Comment on the morphology of the erythrocytes.
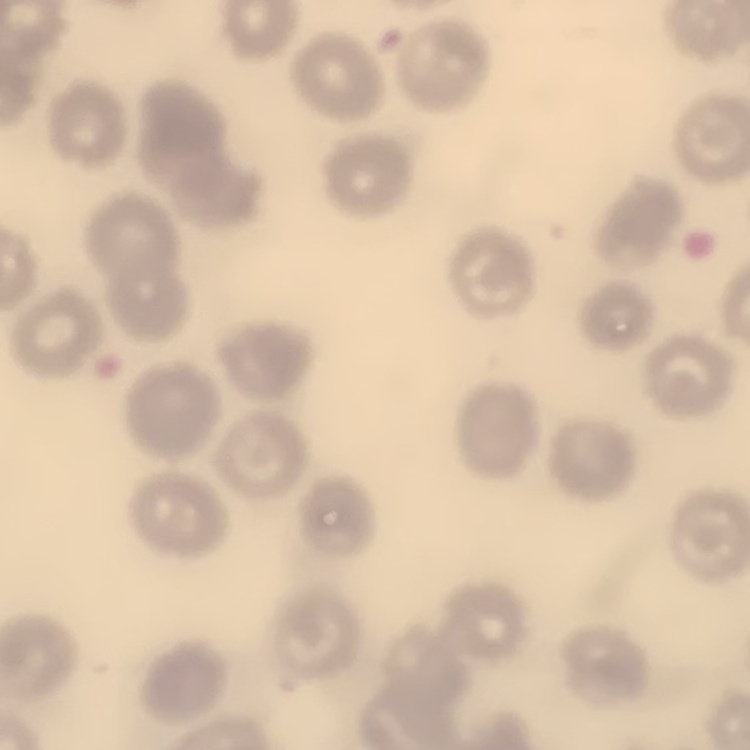

They show no rouleaux formation.

One tile cut from a larger photomicrograph. Stained with either Field's or Giemsa. Thin blood film.